Describe the morphology of the red blood cells.
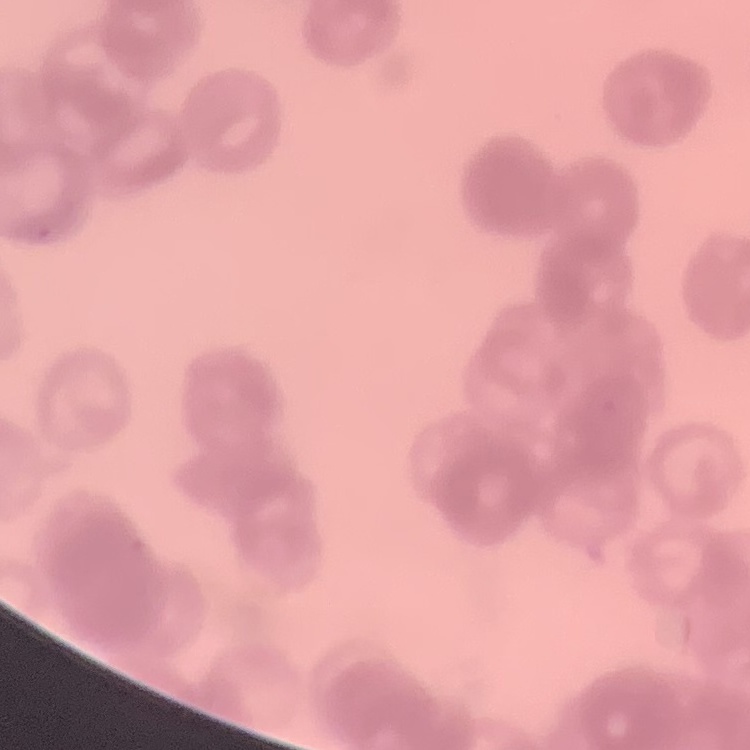

Rouleaux formation.

Thin blood smear. Stained with either Field's or Giemsa. One tile cut from a larger photomicrograph.